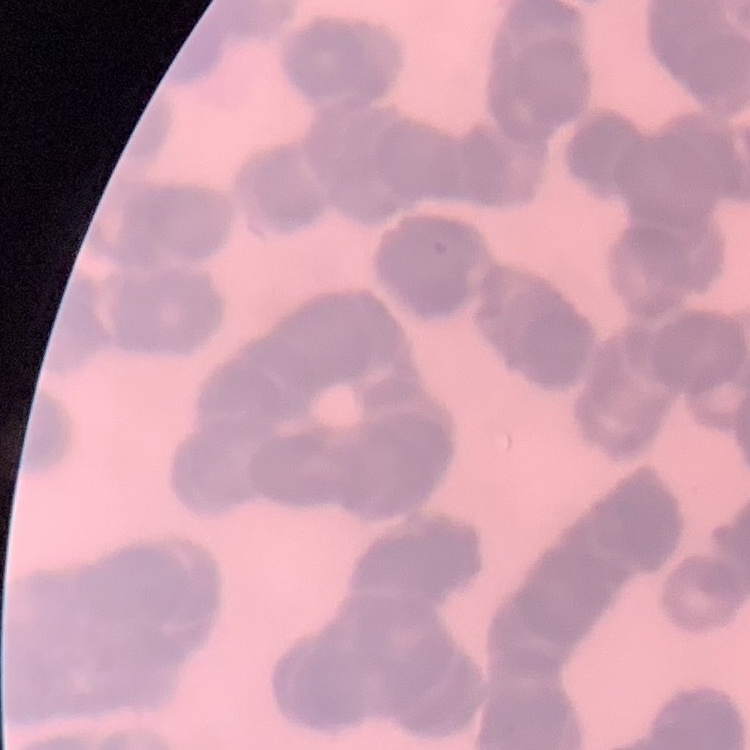 The erythrocytes show rouleaux formation. One tile cut from a larger photomicrograph. Thin peripheral smear. Stained with either Field's or Giemsa.